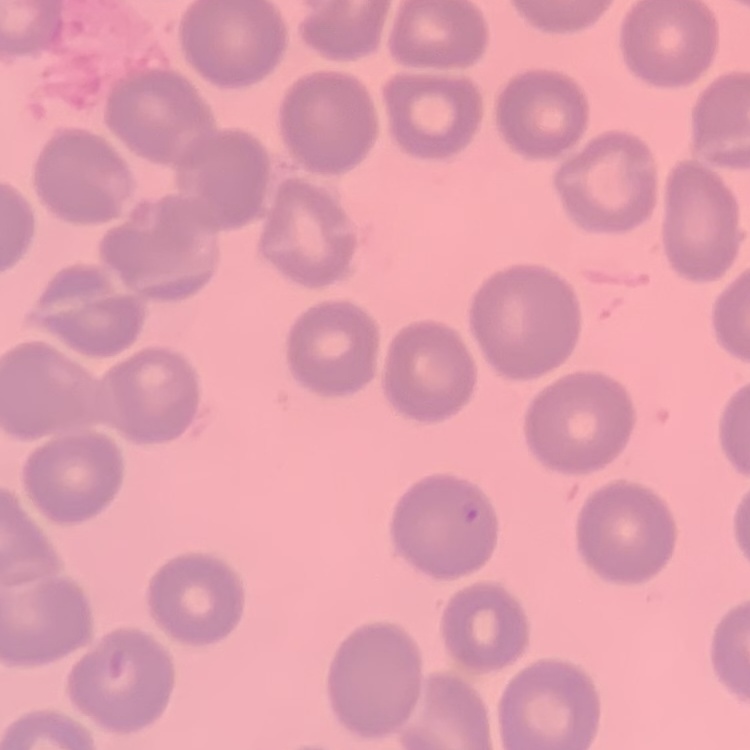

The red blood cells exhibit no rouleaux formation. Thin blood film. Square crop of a larger photomicrograph. Field's or Giemsa stain.